Classify this cell by malaria status.
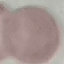
Uninfected.

Thin smear of blood. Photographed with a smartphone camera at the microscope eyepiece. Giemsa-stained preparation. Cell patch, automatically extracted from a larger field of view and resized to 64 × 64 pixels.